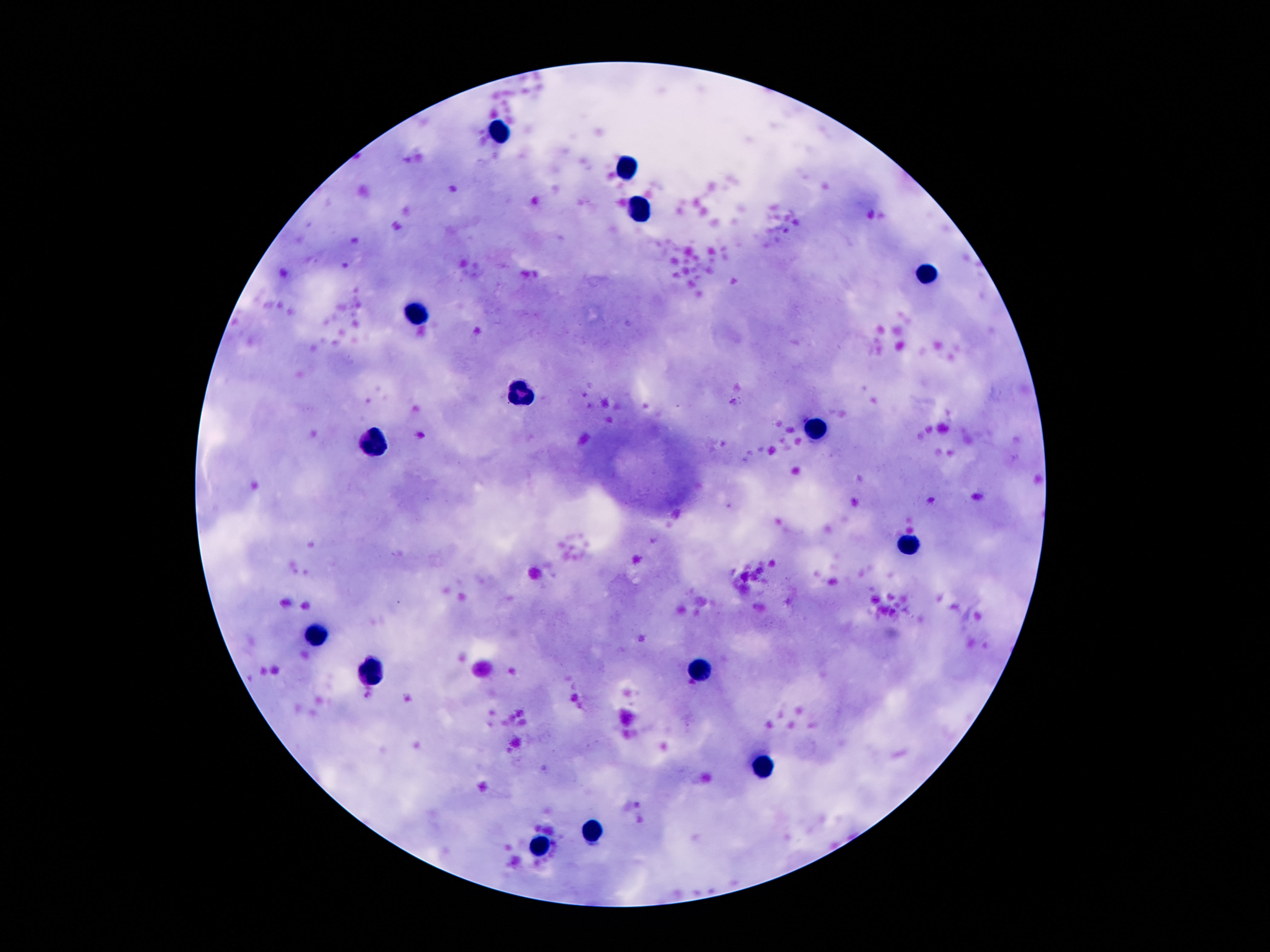 Approximate centers as (x, y) in pixels. Leukocyte locations: (498, 133), (625, 168), (641, 209), (925, 270), (416, 313), (523, 390), (812, 431), (373, 446), (909, 545), (316, 633), (698, 670), (375, 674), (764, 770), (596, 832), (537, 849). One field from this slide. Photographed through the microscope eyepiece with a smartphone camera. Image is 1270×952 pixels. Thick peripheral-blood smear. Patient malaria status: negative. 100x magnification. Giemsa-stained preparation.